Evaluate for Plasmodium parasites.
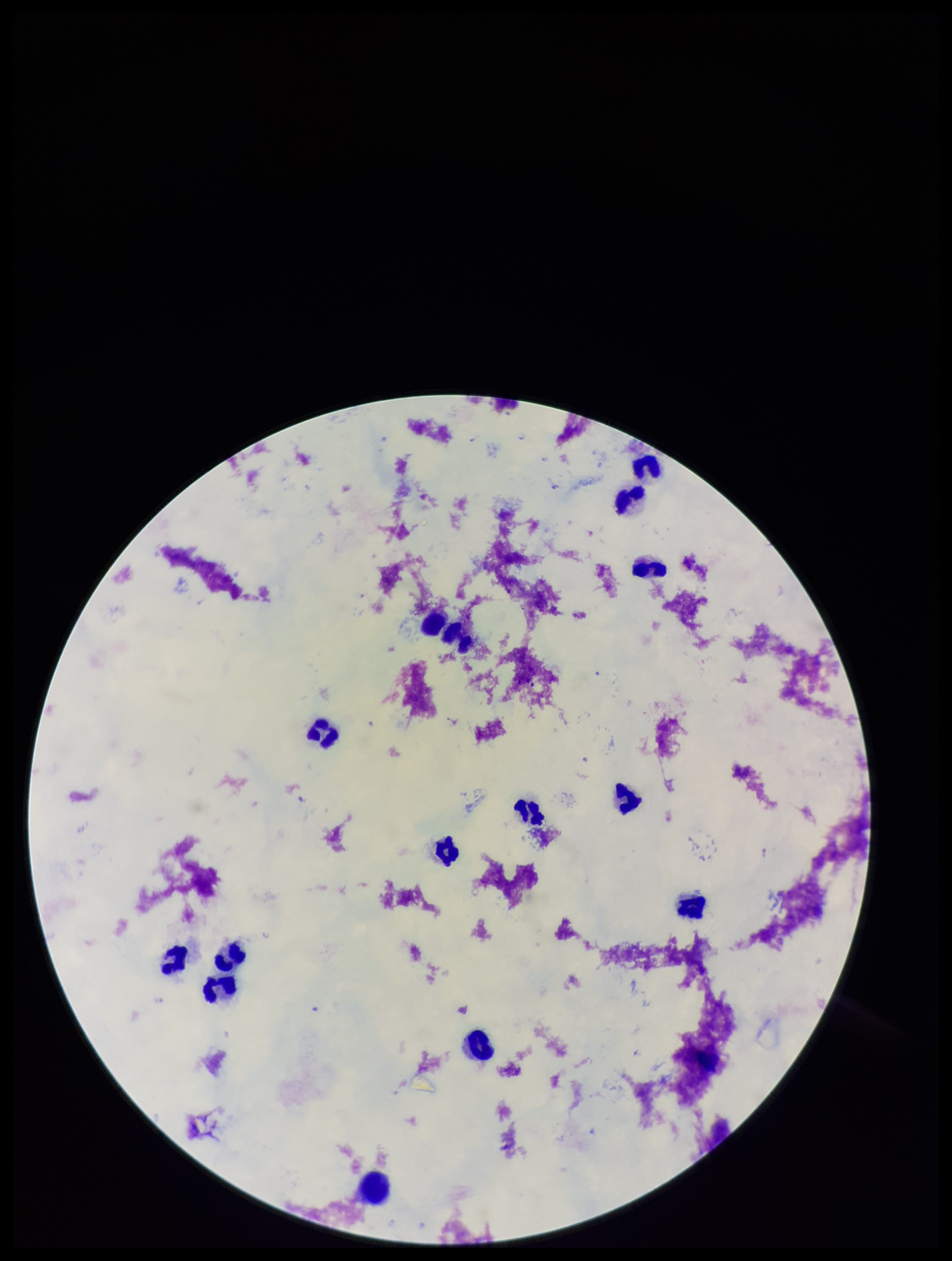

Detected.

Summary:
  - Patient malaria status: infected
  - Species reported for this patient: Plasmodium falciparum
  - Capture: smartphone photograph through the microscope eyepiece
  - Leukocyte count: 15
  - Parasite count: 4
  - Field of view: one from this slide
  - Preparation: thick
  - Stain: Giemsa
  - Image size: 952×1261 pixels